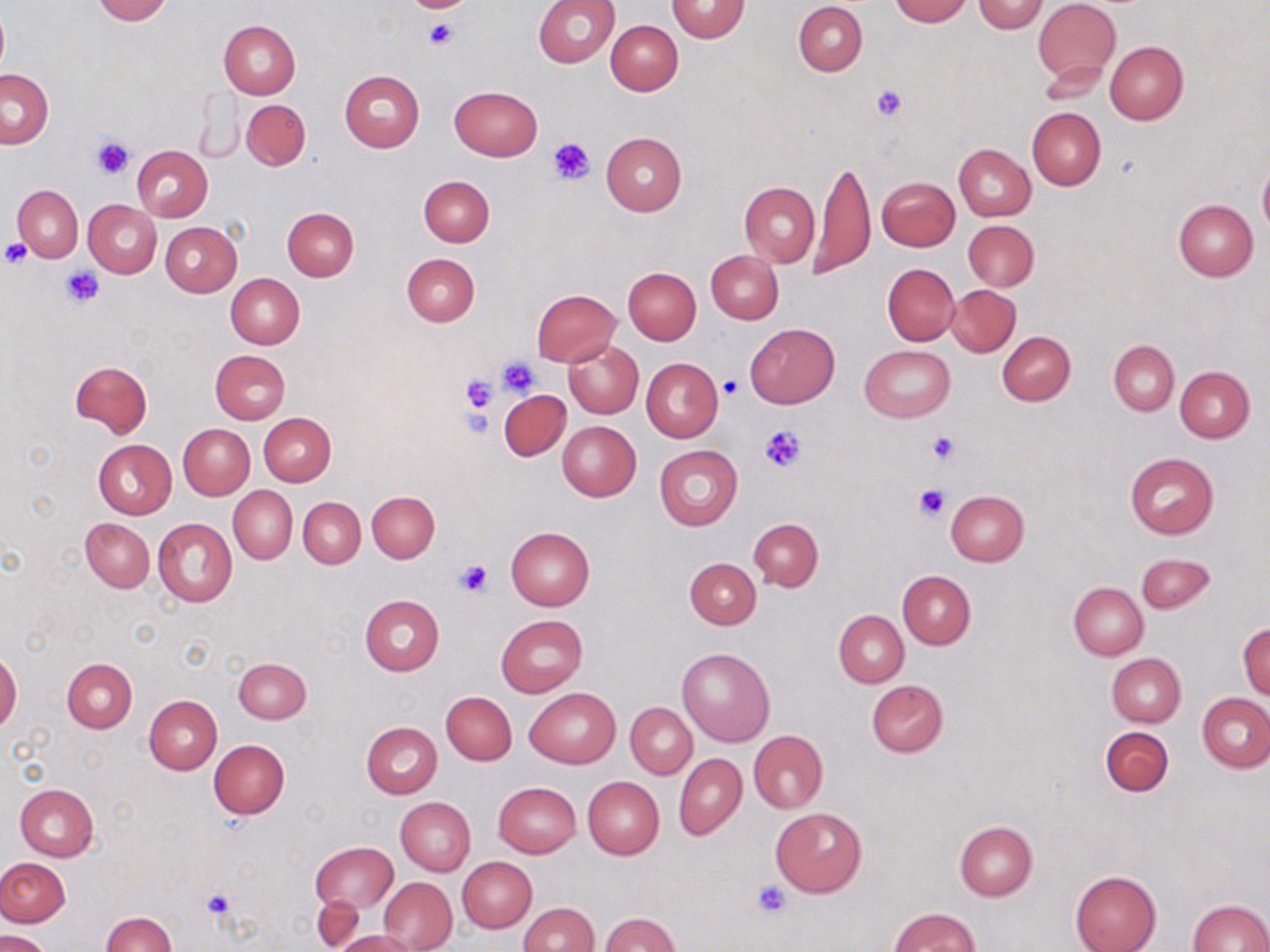
Summary:
  - Coordinate format: approximate bounding boxes as (x1,y1)-(x2,y2) corner pairs in pixels
  - Uninfected red blood cell locations: (92,0)-(171,24), (533,0)-(619,68), (666,0)-(750,43), (889,0)-(970,24), (973,1)-(1048,33), (1034,1)-(1120,82), (794,2)-(867,76), (0,8)-(9,79), (218,19)-(300,98), (606,20)-(683,96), (1105,42)-(1187,124), (1038,63)-(1109,106), (1,68)-(53,148), (339,70)-(425,151), (450,86)-(542,160), (196,88)-(247,163), (241,99)-(310,170), (1027,108)-(1105,189), (601,132)-(686,216), (954,143)-(1035,221), (132,145)-(212,221), (813,159)-(874,279), (1258,163)-(1270,237), (811,172)-(955,260), (418,176)-(494,246), (877,177)-(959,251), (740,181)-(820,268), (12,185)-(83,261), (1173,199)-(1258,281), (84,200)-(162,278), (282,207)-(359,281), (963,220)-(1039,290), (161,221)-(241,296), (706,250)-(783,323), (401,254)-(479,327), (882,264)-(959,346), (623,267)-(700,344), (226,273)-(304,349), (946,285)-(1021,357), (532,289)-(620,367), (745,323)-(839,408), (997,332)-(1075,405), (563,339)-(643,418), (1109,340)-(1179,414), (859,344)-(955,421), (211,350)-(290,424), (640,358)-(723,443), (71,360)-(152,438), (1175,365)-(1255,442), (499,389)-(569,460), (259,412)-(336,486), (558,421)-(641,502), (179,424)-(255,499), (94,439)-(176,519), (655,444)-(743,530), (1125,453)-(1219,539), (229,486)-(297,564), (945,490)-(1028,566), (367,491)-(439,562), (299,497)-(365,567), (152,517)-(237,607), (81,518)-(154,592), (749,518)-(823,591), (506,526)-(595,609), (1136,553)-(1213,613), (684,557)-(761,629), (898,570)-(975,649), (1068,583)-(1147,660), (360,594)-(444,675), (834,610)-(908,687), (496,615)-(587,697), (1238,623)-(1270,698), (677,647)-(774,746), (0,651)-(22,733), (1106,653)-(1186,727), (62,657)-(136,732), (234,657)-(311,724), (866,681)-(949,757), (525,687)-(620,768), (442,692)-(516,764), (1197,694)-(1270,772), (144,695)-(222,773), (626,703)-(697,778), (362,721)-(442,798), (1100,726)-(1173,796), (749,731)-(828,812), (209,739)-(288,819), (674,753)-(746,841), (582,776)-(664,859), (492,782)-(580,858), (9,784)-(84,927), (14,784)-(99,860), (395,797)-(476,875), (770,807)-(867,897), (954,821)-(1037,901), (311,842)-(397,917), (458,856)-(536,932), (1,857)-(70,927), (1070,870)-(1162,952), (379,877)-(456,950), (314,895)-(364,951), (1187,900)-(1270,951), (518,902)-(599,952), (888,907)-(979,951), (101,911)-(175,952), (600,913)-(678,951), (2,930)-(52,952), (332,930)-(422,952)
  - Platelet locations: (407,0)-(470,13), (424,18)-(460,50), (870,85)-(906,121), (90,133)-(135,179), (547,137)-(595,186), (0,238)-(34,267), (62,267)-(104,308), (496,355)-(540,398), (461,374)-(497,415), (720,375)-(743,399), (761,424)-(806,473), (927,431)-(959,464), (914,484)-(950,520), (452,558)-(495,598), (752,880)-(794,918), (201,887)-(237,921)
  - Slide-level diagnosis: no evidence of blood parasites
  - Stain: May-Grünwald-Giemsa
  - Image size: 1270×952 pixels
  - Preparation: thin blood film
  - Modality: light microscopy
  - Field of view: single
  - Magnification: 1000x